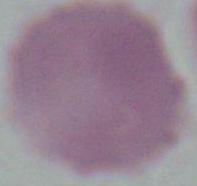

magnification = 1000x
identification = red blood cell
modality = photomicrograph